Report the malaria status of this cell.
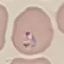
Parasitized.

capture = smartphone camera at the microscope eyepiece
preparation = thin smear
stain = Giemsa
image type = automatically extracted cell patch, resized to 64 × 64 pixels